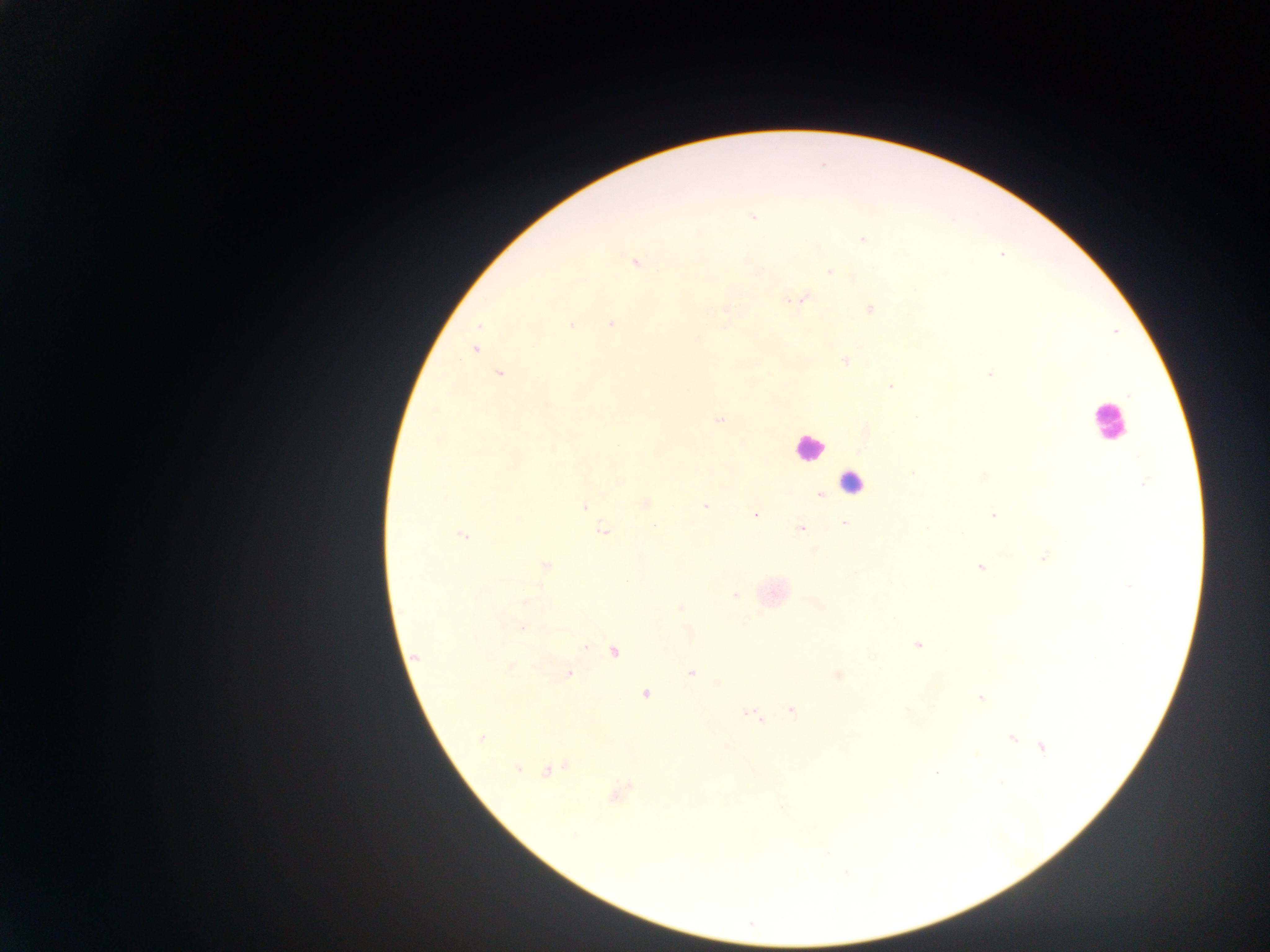

Approximate centers as {x, y} in pixels. Leukocyte locations: {1108, 421}, {808, 447}, {856, 478}. Malaria parasite locations: {752, 216}, {863, 240}, {634, 261}, {756, 270}, {829, 271}, {801, 299}, {871, 309}, {725, 310}, {611, 323}, {571, 325}, {697, 340}, {474, 350}, {845, 361}, {499, 373}, {990, 374}, {891, 387}, {718, 420}, {912, 473}, {983, 476}, {619, 482}, {1144, 483}, {820, 494}, {645, 503}, {584, 506}, {705, 506}, {755, 515}, {993, 515}, {845, 523}, {801, 529}, {603, 531}, {463, 535}, {814, 549}, {1043, 557}, {545, 565}, {980, 567}, {855, 573}, {1129, 587}, {735, 595}, {817, 603}, {681, 607}, {522, 627}, {688, 631}, {917, 644}, {584, 647}, {615, 652}, {415, 656}, {511, 666}, {691, 673}, {569, 674}, {837, 675}, {719, 683}, {646, 694}, {981, 698}, {791, 710}, {753, 716}, {481, 737}, {1012, 737}, {1043, 747}, {517, 769}, {548, 771}, {936, 771}, {619, 793}. One field of view. Sample from Ghana. Photographed through a microscope with a mobile-phone camera. Thick blood smear. Image is 1270×952 pixels.